Assess this cell for malaria.
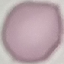

It is uninfected.

Thin blood smear. Acquired by smartphone through the microscope eyepiece. Cell patch, automatically extracted from a larger field of view and resized to 64 × 64 pixels. Giemsa-stained preparation.